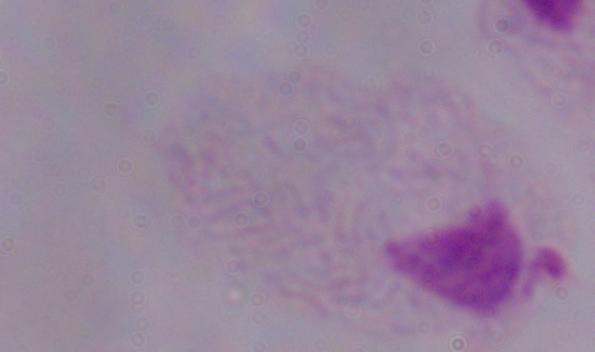

A trichomonad is shown. Photomicrograph. Captured at 1000x magnification.